State which cell type is depicted.
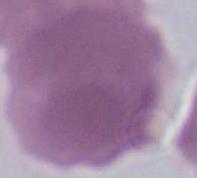
This is an erythrocyte.

modality: photomicrograph
magnification: 1000x